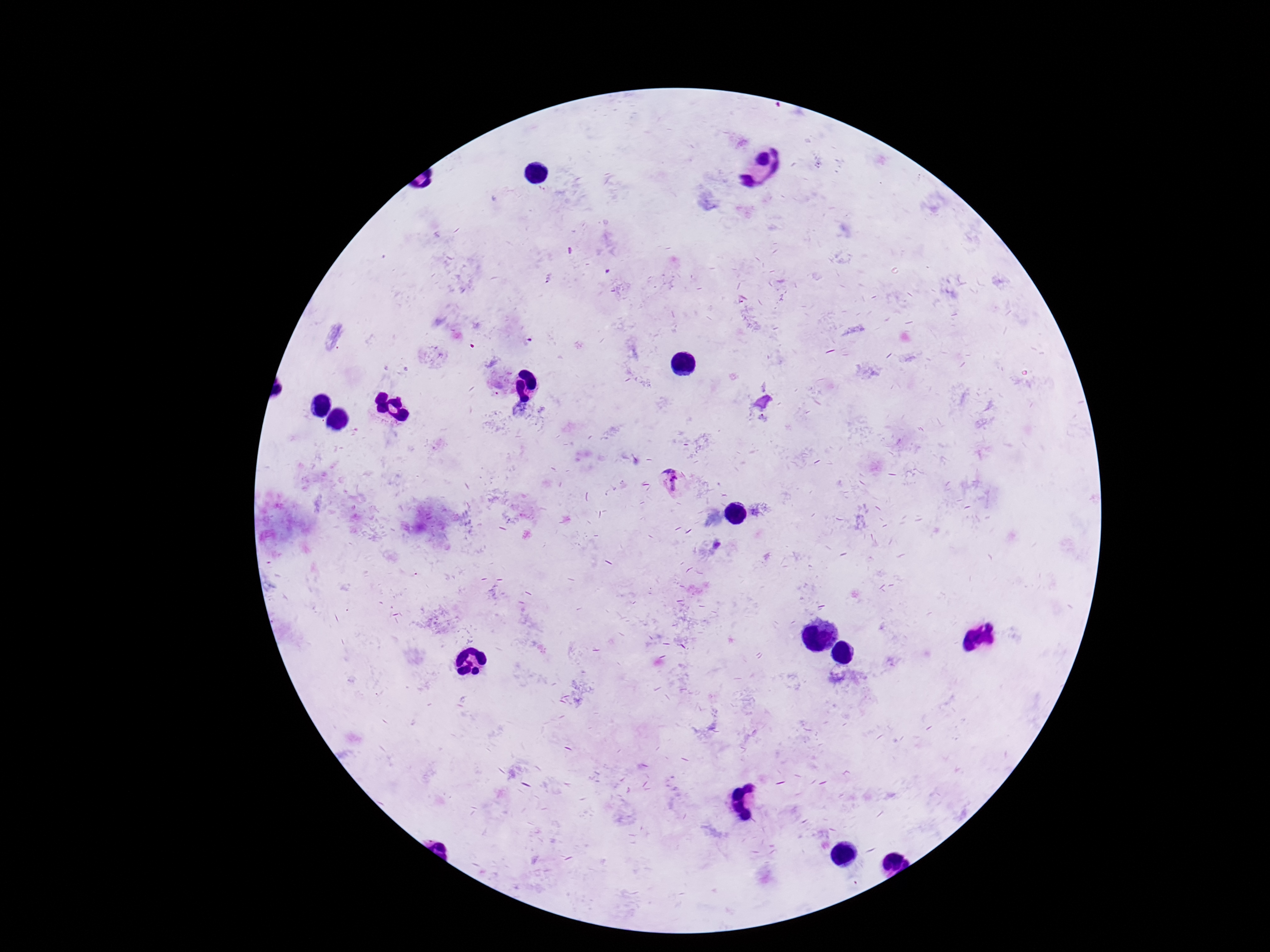
Approximate object centers, in pixels from the top-left corner. Plasmodium parasite locations: (x=671, y=482). Single field of view. Patient malaria status: positive. Smartphone photograph taken through the microscope eyepiece. Image is 1270×952 pixels. 100x magnification. Giemsa stain. Thick peripheral-blood smear.